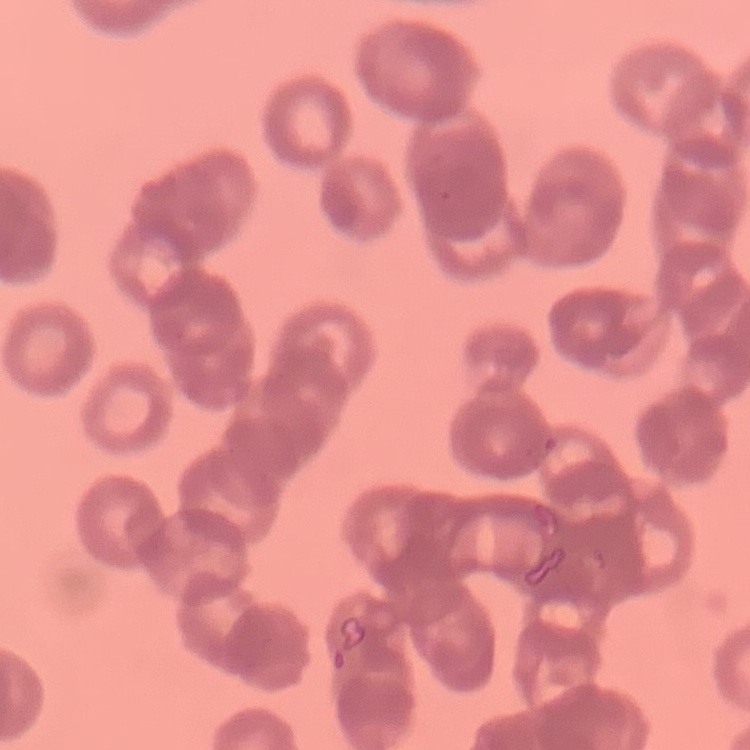
The erythrocytes exhibit rouleaux formation. Square crop of a larger photomicrograph. Field's or Giemsa stain. Thin peripheral smear.